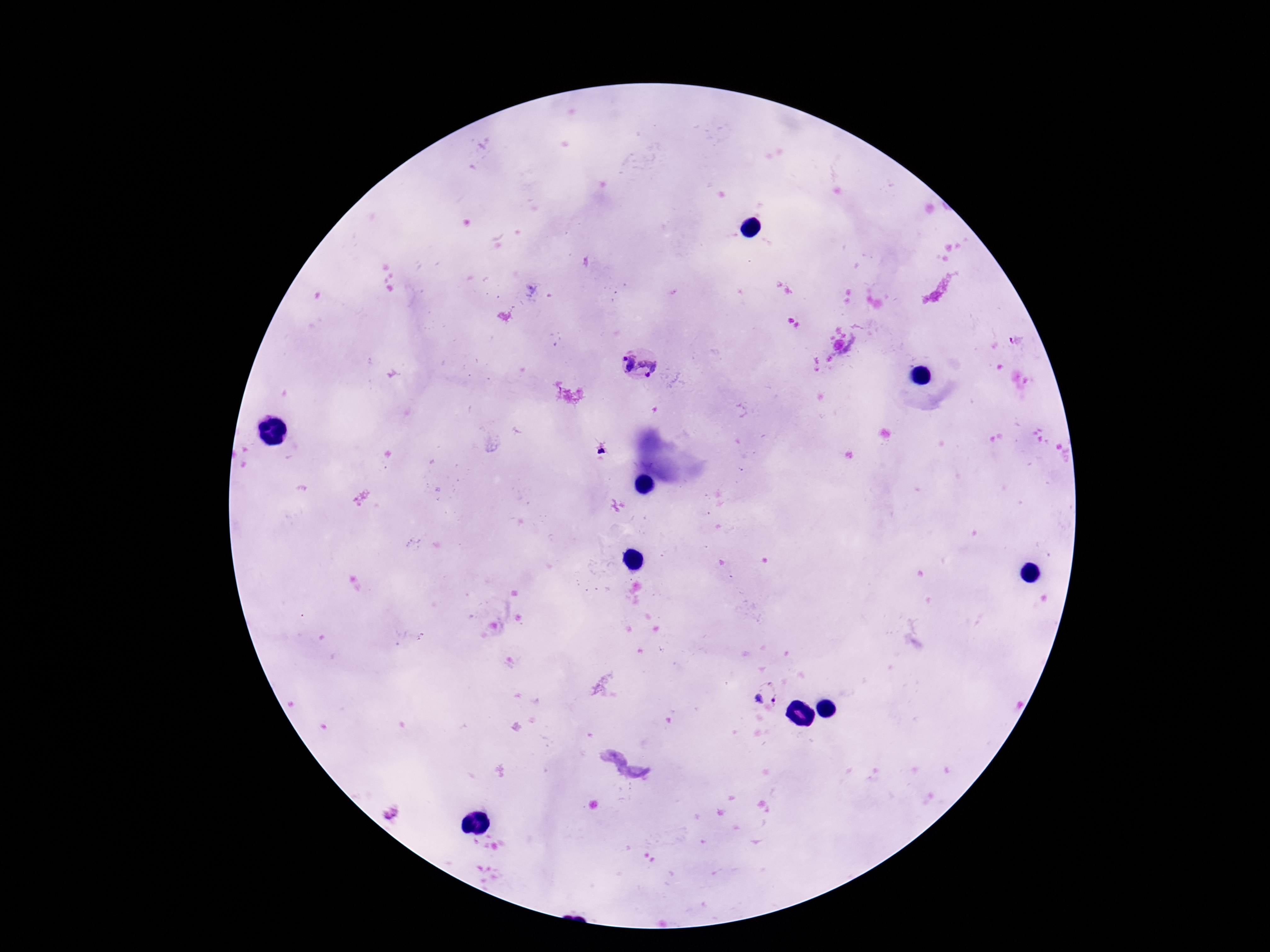

Approximate object centers, in pixels from the top-left corner.
Summary:
  - Plasmodium parasite locations: (x=625, y=362), (x=649, y=366), (x=764, y=696)
  - Field of view: one from this slide
  - Patient malaria status: positive
  - Magnification: 100x
  - Preparation: thick blood smear
  - Image size: 1270×952 pixels
  - Capture: smartphone camera through the microscope eyepiece
  - Stain: Giemsa